Locate every malaria parasite.
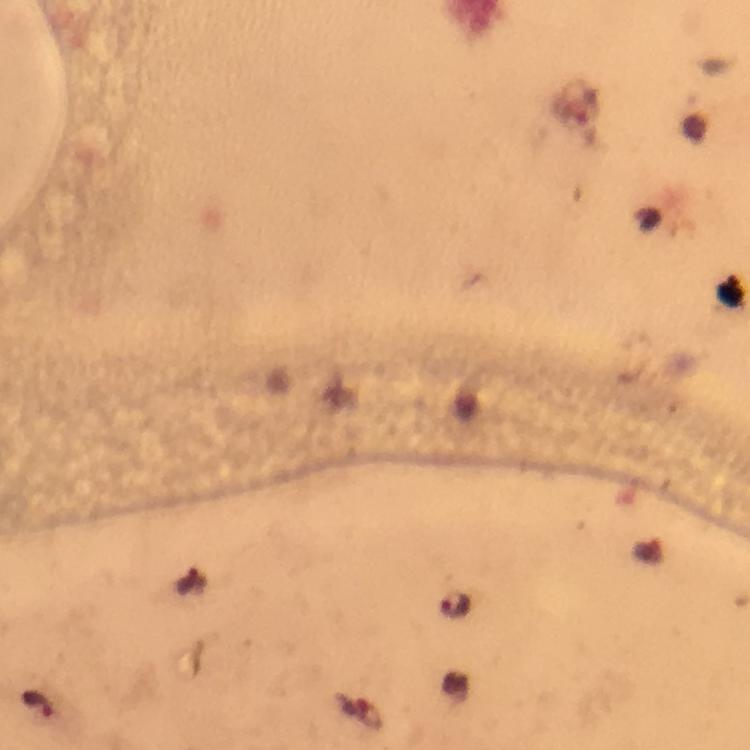

Approximate centers as {x, y} in pixels.
Malaria parasites: {456, 605}, {40, 704}.

cropped from = a single field of view
immersion oil = used
capture = smartphone camera through the microscope
image size = 750×750 pixels
stain = Giemsa
preparation = thick smear
context = from a malaria diagnostic workup
magnification = 100x